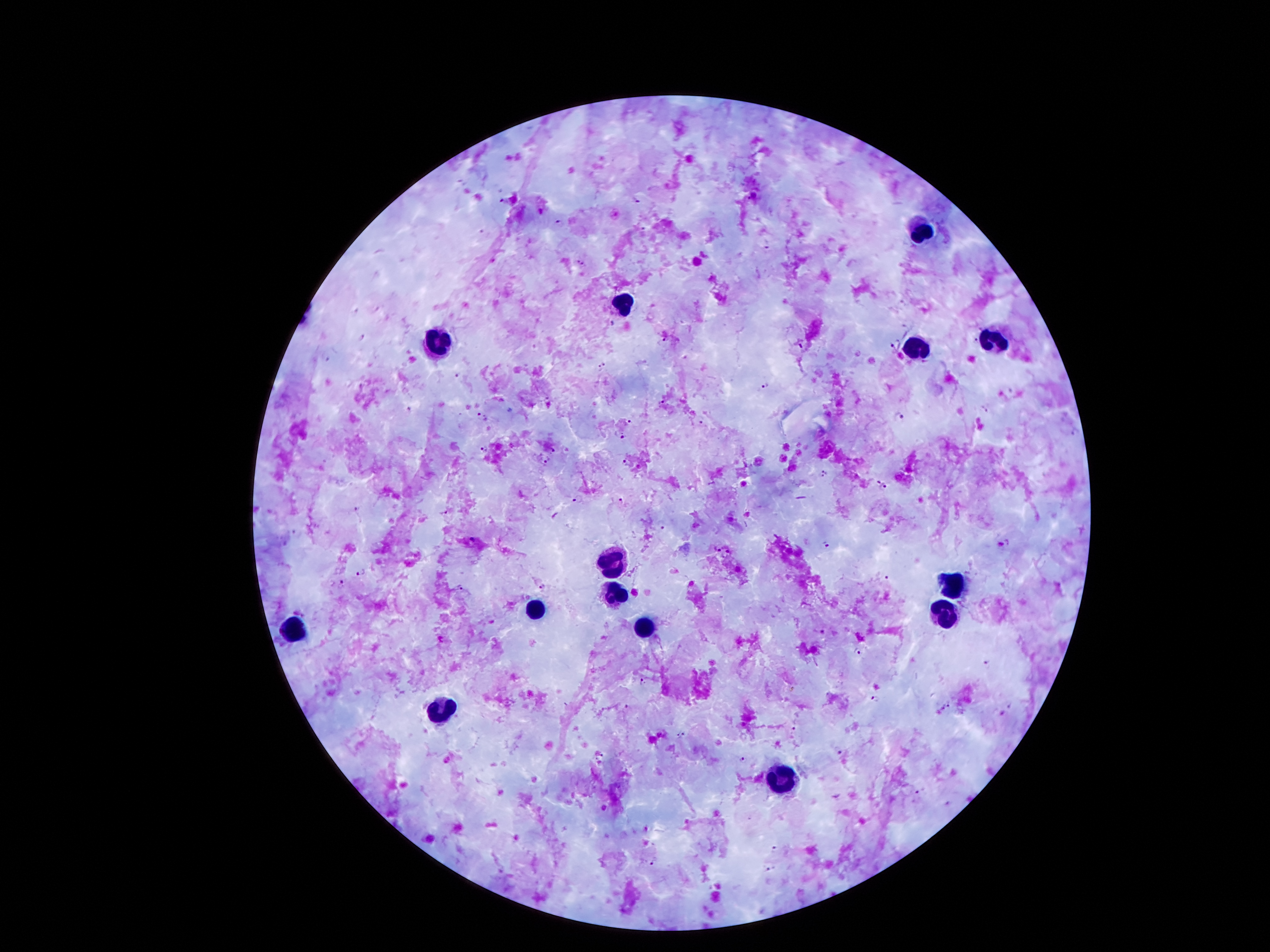

coordinate format = approximate centers as {x, y} in pixels
leukocyte locations = {924, 229}, {625, 303}, {437, 344}, {1002, 344}, {918, 348}, {615, 563}, {955, 582}, {611, 592}, {535, 608}, {945, 610}, {646, 627}, {293, 631}, {443, 709}, {781, 780}
Plasmodium parasite locations = {752, 196}, {636, 200}, {559, 221}, {766, 245}, {573, 259}, {585, 267}, {613, 325}, {361, 338}, {665, 339}, {977, 340}, {894, 347}, {324, 355}, {602, 365}, {458, 374}, {767, 386}, {661, 402}, {408, 407}, {985, 408}, {481, 416}, {900, 416}, {631, 423}, {703, 425}, {618, 436}, {484, 448}, {546, 462}, {624, 462}, {823, 474}, {875, 480}, {886, 488}, {578, 498}, {621, 500}, {356, 508}, {444, 514}, {662, 525}, {828, 544}, {1008, 544}, {717, 549}, {358, 571}, {884, 580}, {343, 581}, {542, 587}, {460, 588}, {857, 649}, {986, 662}, {642, 683}, {875, 698}, {949, 704}, {626, 707}, {793, 727}, {681, 735}, {836, 750}, {602, 756}, {742, 758}, {918, 790}, {774, 850}, {653, 863}, {768, 870}
field of view = one from this slide
patient malaria status = positive for Plasmodium falciparum
image size = 1270×952 pixels
magnification = 100x
capture = smartphone camera through the microscope eyepiece
stain = Giemsa
preparation = thick peripheral-blood smear